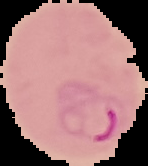 Image is 148×166 pixels. The area outside the segmented cell region is set to black. From a thin blood smear. Malaria status: parasitized.